Identify the cell.
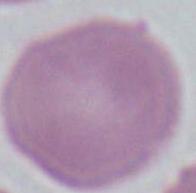
This is an erythrocyte.

Summary:
  - Magnification: 1000x
  - Modality: photomicrograph